Comment on the morphology of the red blood cells.
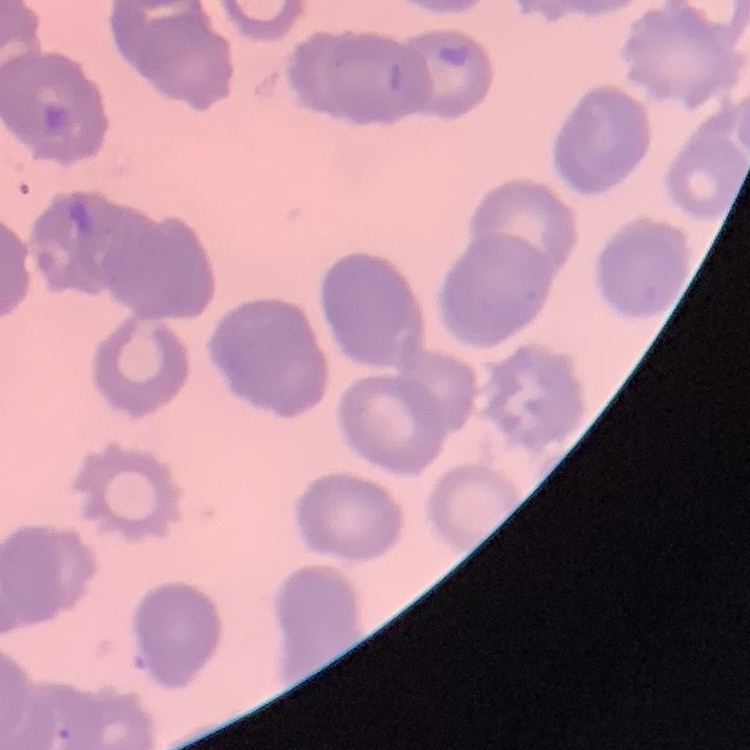
Rouleaux formation.

Summary:
  - Stain: Field's or Giemsa
  - Preparation: thin blood film
  - Image type: square crop of a larger photomicrograph